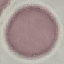

Summary:
  - Result: no malaria parasites seen
  - Preparation: thin blood film
  - Image type: automatically extracted cell patch, resized to 64 × 64 pixels
  - Capture: smartphone camera at the microscope eyepiece
  - Stain: Giemsa